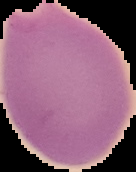
malaria_status: parasitized
image_type: segmented cell region on a black background
image_size: 136×172 pixels
preparation: thin blood film